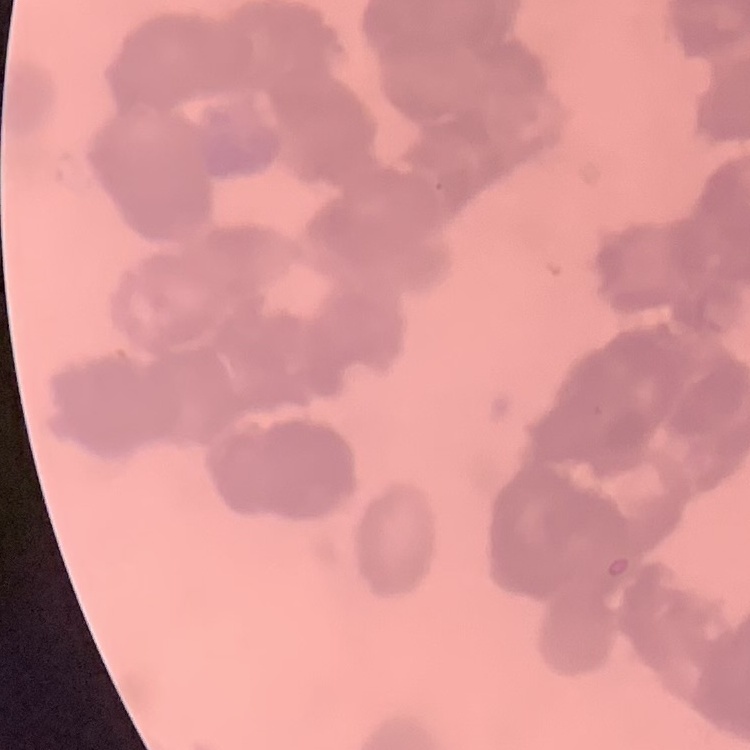

Summary:
  - Erythrocyte morphology: rouleaux formation
  - Stain: Field's or Giemsa
  - Image type: one tile cut from a larger photomicrograph
  - Preparation: thin peripheral smear